Report the malaria status.
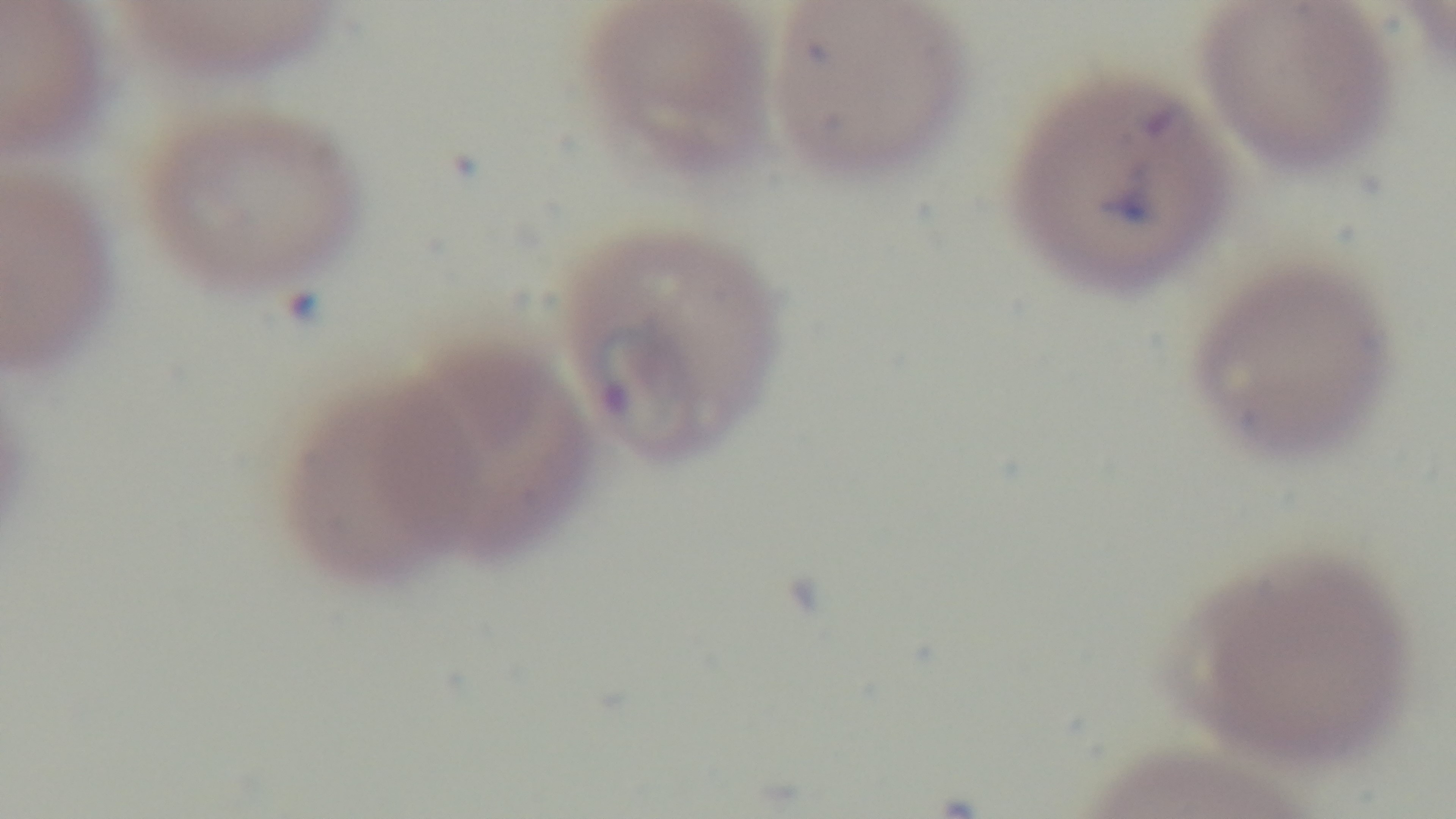
Infected.

modality = light microscopy
stain = Giemsa
preparation = thin smear
objective = 100x oil immersion
field of view = one from the slide
capture = mounted 4K digital camera